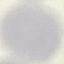
Summary:
  - Malaria status: uninfected
  - Capture: smartphone camera at the microscope eyepiece
  - Preparation: thin blood film
  - Stain: Giemsa
  - Image type: automatically extracted cell patch, resized to 64 × 64 pixels